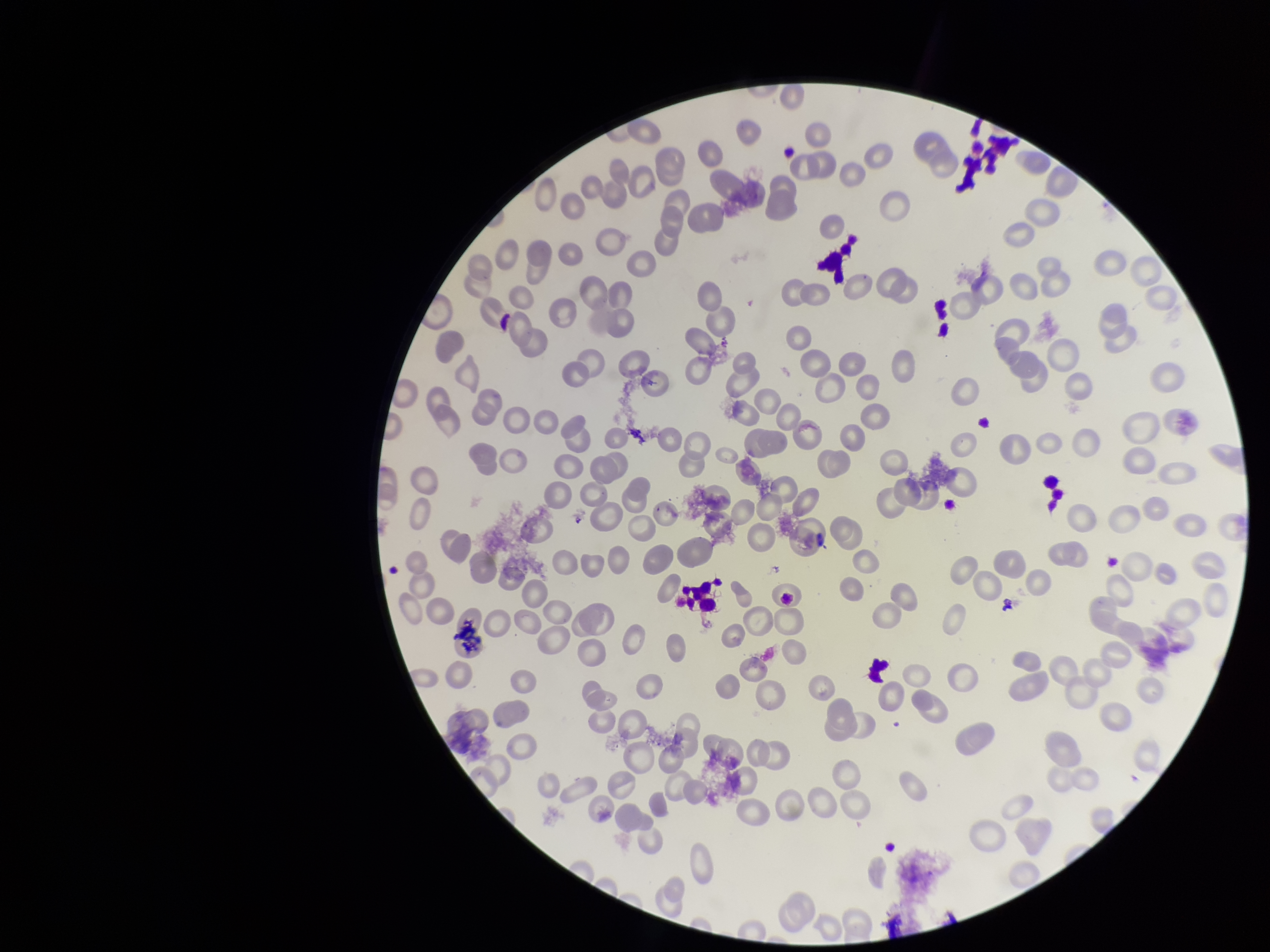
Summary:
  - Image size: 1270×952 pixels
  - Capture: smartphone photograph through the microscope eyepiece
  - Stain: Giemsa
  - Parasitized red blood cell count: 0
  - Parasitized red blood cells: none seen
  - Patient malaria status: negative
  - Field of view: one from this slide
  - Red blood cell count: 165
  - Preparation: thin